Locate and identify every blood parasite.
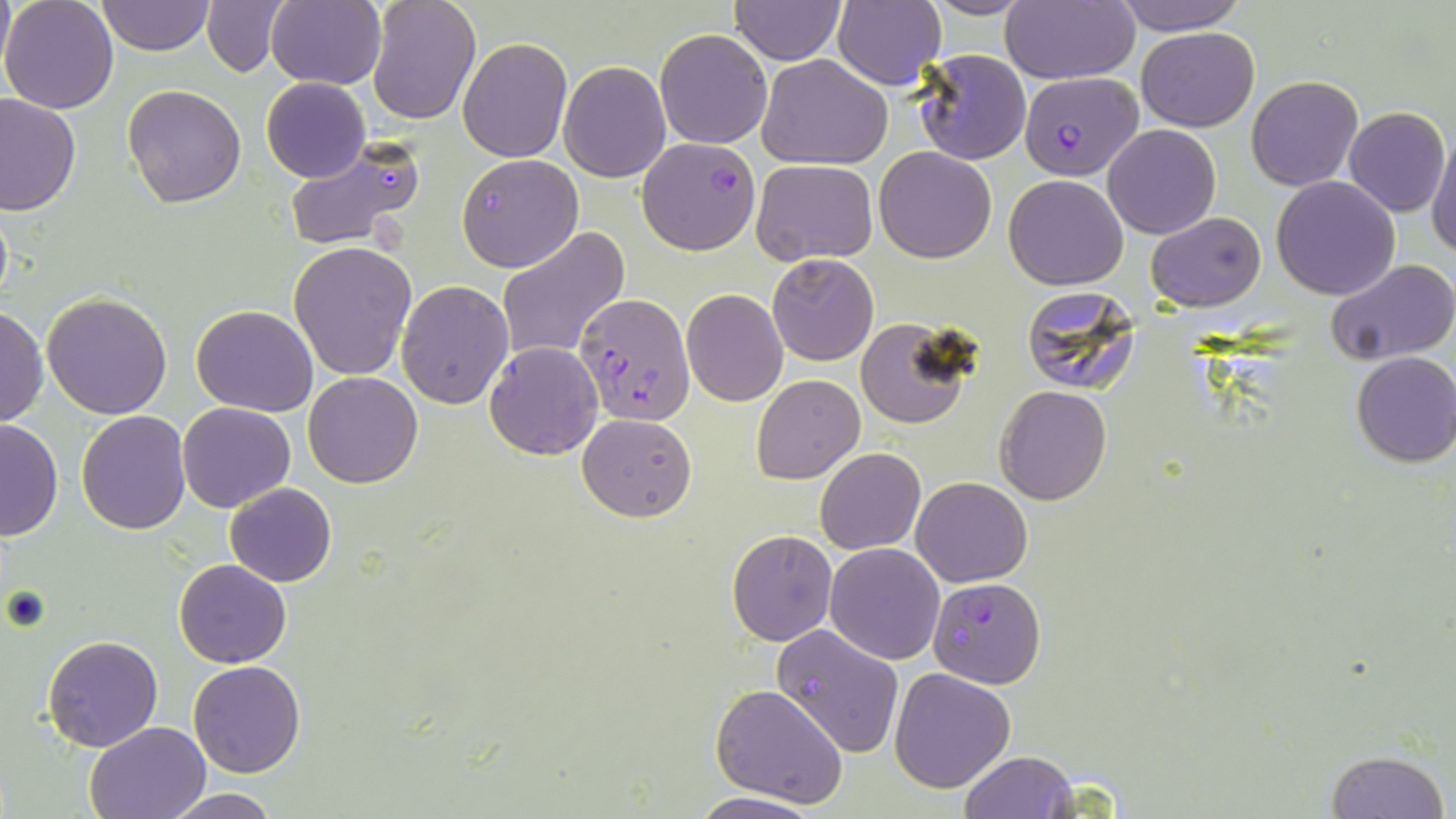

Approximate bounding boxes as (x1,y1)-(x2,y2) corner pairs in pixels.
Plasmodium falciparum-infected red blood cells (subset): (1018,72)-(1140,180), (636,138)-(761,256), (573,293)-(696,427).
No Plasmodium ovale, Plasmodium malariae, Plasmodium vivax, Babesia divergens, or Trypanosoma brucei observed.

Summary:
  - Uninfected red blood cell locations (subset): (0,0)-(120,113), (98,0)-(214,55), (264,0)-(386,90), (367,0)-(482,123), (727,0)-(847,64), (918,0)-(1038,20), (1001,0)-(1137,86), (1112,0)-(1249,35), (202,2)-(286,76), (832,2)-(946,88), (1136,27)-(1259,130), (655,28)-(772,149), (458,37)-(573,163), (911,48)-(1033,165), (755,53)-(892,170), (558,60)-(672,183), (1246,75)-(1363,190), (261,77)-(371,182), (122,83)-(248,208), (0,94)-(80,217), (1343,105)-(1451,217), (1102,123)-(1221,239), (1427,126)-(1456,259), (283,136)-(428,252), (874,147)-(998,263), (456,155)-(584,272), (752,159)-(876,266), (1004,174)-(1128,290), (1271,176)-(1402,300), (1146,212)-(1267,313), (496,226)-(629,361), (288,240)-(418,380), (767,253)-(878,366), (1325,258)-(1456,366), (394,280)-(514,409), (1020,286)-(1144,395), (681,288)-(787,406), (41,293)-(173,419), (1,303)-(48,429), (191,304)-(319,416), (853,318)-(976,431), (483,341)-(603,461), (1350,351)-(1456,469), (303,371)-(424,488), (751,374)-(865,484), (993,386)-(1112,505), (176,402)-(298,513), (76,410)-(191,534), (577,413)-(697,521), (0,417)-(63,542), (814,447)-(925,554), (912,477)-(1033,586), (224,482)-(337,586), (727,530)-(838,646), (824,543)-(945,664), (173,559)-(293,668), (772,623)-(904,758), (43,635)-(163,752), (188,660)-(306,778), (890,667)-(1017,793), (710,683)-(848,807), (83,721)-(212,819), (1325,749)-(1450,819), (956,751)-(1079,819), (163,789)-(279,818), (690,792)-(821,818)
  - Slide-level diagnosis: Plasmodium falciparum
  - Stain: May-Grünwald-Giemsa
  - Modality: optical microscopy
  - Image size: 1456×819 pixels
  - Field of view: one of a larger specimen
  - Magnification: 1000x
  - Preparation: thin blood smear